Report the malaria status of this cell.
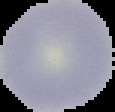
It is uninfected.

Summary:
  - Preparation: thin blood smear
  - Image size: 115×112 pixels
  - Image type: segmented cell region with the area outside set to black